Give the position of every leukocyte visible.
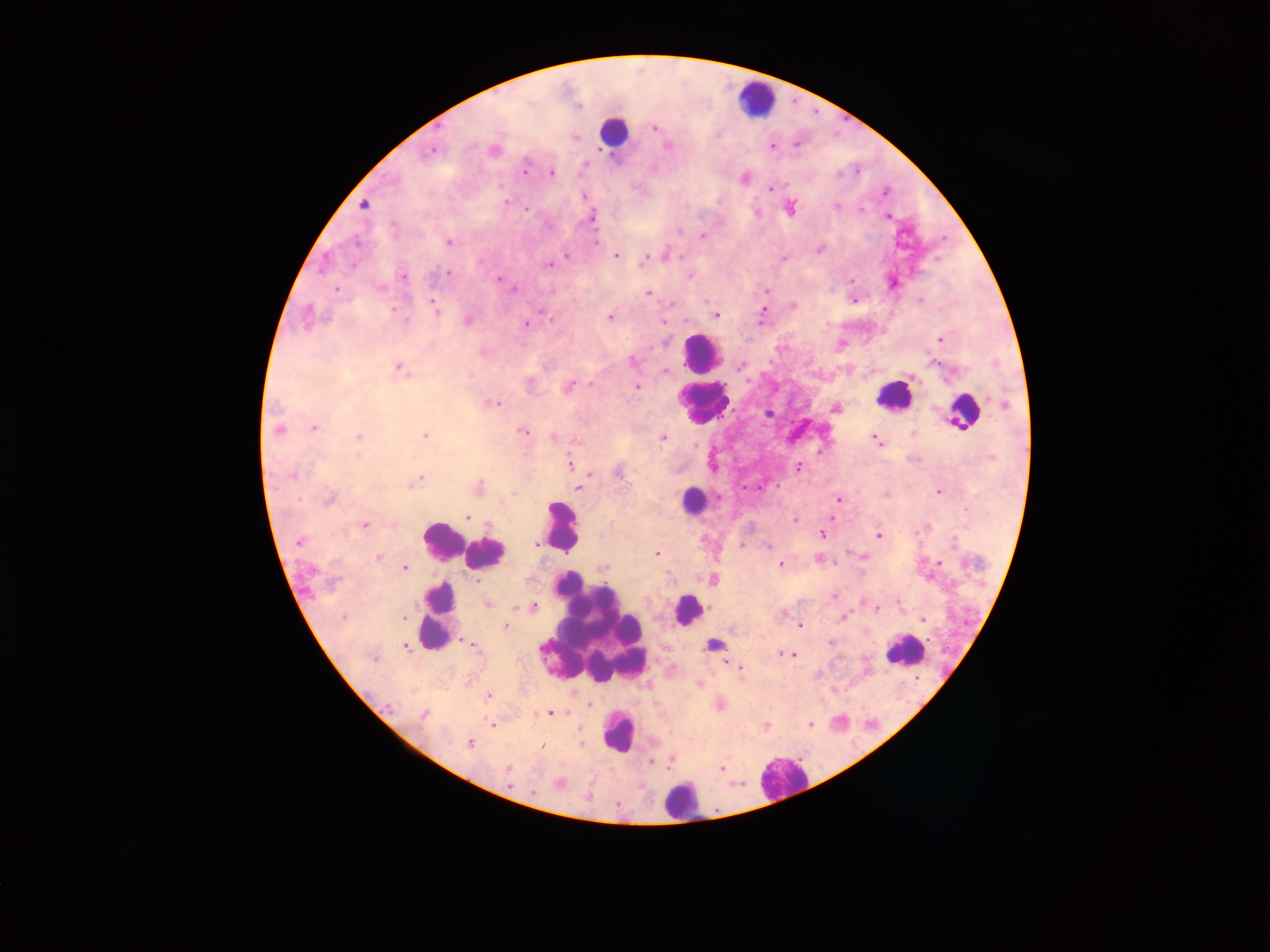

Approximate centers as (x, y) in pixels.
Leukocytes: (757, 98), (613, 132), (701, 353), (893, 395), (702, 403), (964, 411), (693, 500), (560, 526), (441, 542), (484, 552), (437, 610), (688, 610), (592, 634), (714, 643), (906, 650), (618, 731), (781, 778), (681, 801).

country = Ghana
preparation = thick blood film
malaria parasite locations = approximate centers as (x, y) in pixels: (654, 128), (797, 143), (773, 145), (667, 146), (430, 150), (493, 151), (524, 168), (550, 172), (744, 178), (771, 188), (885, 192), (584, 195), (505, 201), (364, 205), (789, 208), (526, 209), (860, 211), (888, 216), (591, 217), (701, 234), (596, 239), (448, 241), (819, 248), (568, 255), (616, 255), (665, 255), (646, 257), (549, 265), (447, 274), (689, 275), (403, 276), (497, 280), (891, 282), (336, 289), (767, 290), (648, 294), (853, 299), (434, 303), (793, 305), (762, 313), (715, 314), (609, 317), (308, 318), (405, 320), (467, 320), (663, 321), (525, 323), (939, 339), (841, 344), (482, 351), (632, 360), (741, 365), (398, 368), (664, 372), (636, 386), (569, 387), (492, 403), (1004, 405), (835, 407), (769, 413), (314, 427), (278, 430), (522, 431), (915, 433), (425, 435), (359, 437), (553, 437), (662, 437), (875, 439), (576, 441), (569, 465), (798, 468), (619, 472), (589, 474), (291, 475), (415, 481), (577, 487), (479, 488), (939, 491), (884, 494), (329, 498), (838, 500), (466, 517), (794, 519), (829, 519), (363, 525), (925, 528), (822, 534), (877, 534), (300, 542), (535, 542), (742, 545), (769, 546), (656, 553), (862, 556), (379, 557), (820, 559), (939, 562), (780, 564), (602, 567), (404, 569), (713, 579), (479, 583), (834, 595), (488, 604), (532, 607), (876, 608), (782, 613), (403, 616), (842, 617), (924, 619), (800, 624), (506, 625), (831, 642), (471, 644), (406, 646), (787, 654), (725, 663), (731, 665), (741, 670), (698, 684), (487, 697), (590, 704), (719, 704), (550, 713), (423, 715), (810, 723), (493, 725), (765, 726), (470, 744), (543, 746), (671, 757), (650, 760), (721, 767), (506, 769), (559, 783)
field of view = single
image size = 1270×952 pixels
capture = mobile-phone photograph through a microscope